Give the position of every leukocyte visible.
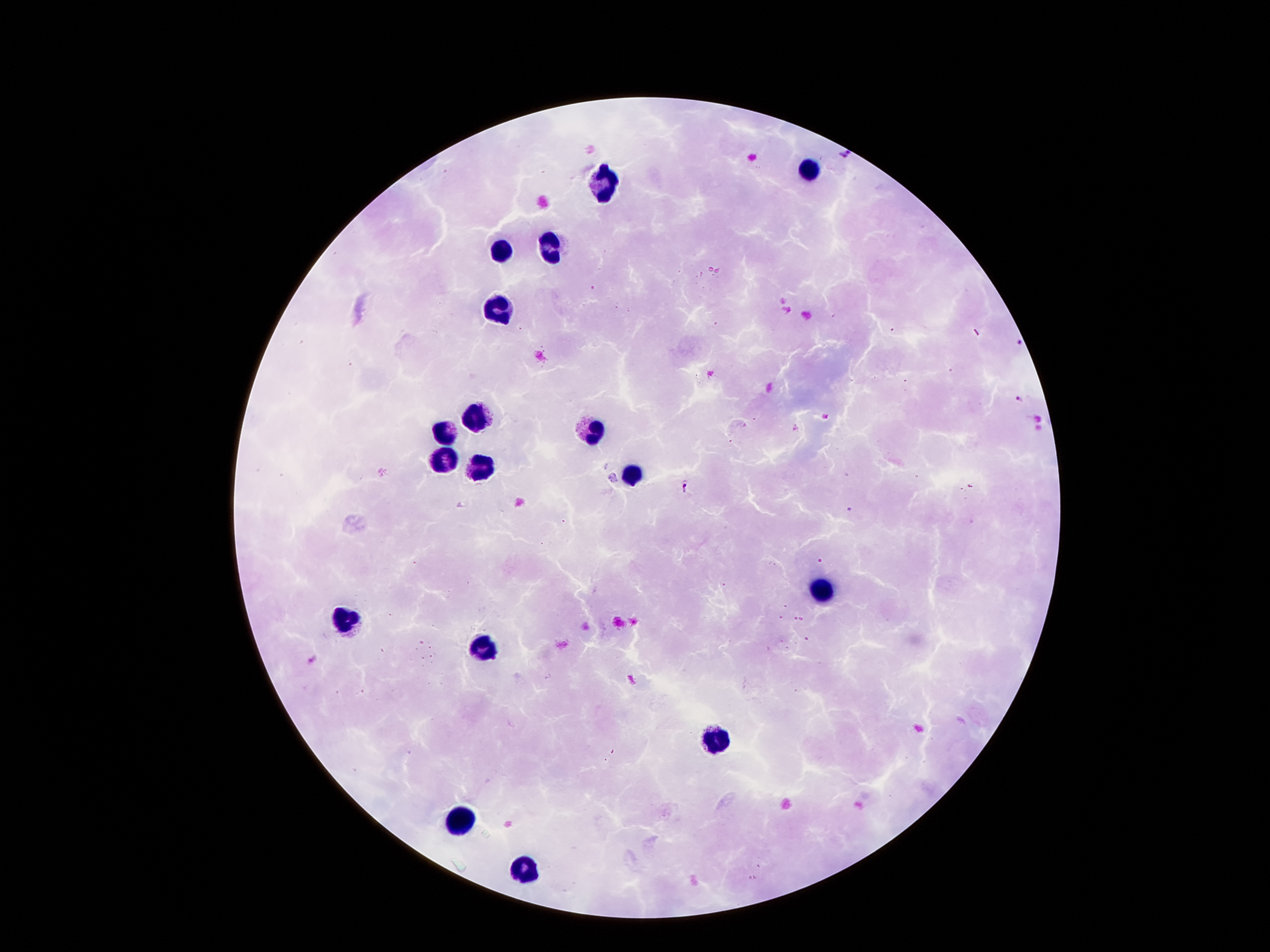

Approximate object centers, in pixels from the top-left corner.
Leukocytes: (x=811, y=170), (x=602, y=183), (x=550, y=248), (x=504, y=251), (x=499, y=311), (x=478, y=419), (x=591, y=430), (x=447, y=433), (x=442, y=459), (x=479, y=467), (x=630, y=472), (x=827, y=590), (x=344, y=619), (x=483, y=650), (x=717, y=742), (x=457, y=816), (x=525, y=871).

image_size: 1270×952 pixels
patient_malaria_status: infected with Plasmodium falciparum
capture: smartphone camera through the microscope eyepiece
magnification: 100x
plasmodium_parasite_locations: 'approximate object centers, in pixels from the top-left corner: (x=845, y=155), (x=1015, y=343), (x=1019, y=400), (x=687, y=488), (x=314, y=659)'
preparation: thick peripheral-blood smear
stain: Giemsa
field_of_view: one from this slide